Assess the morphology of the red blood cells.
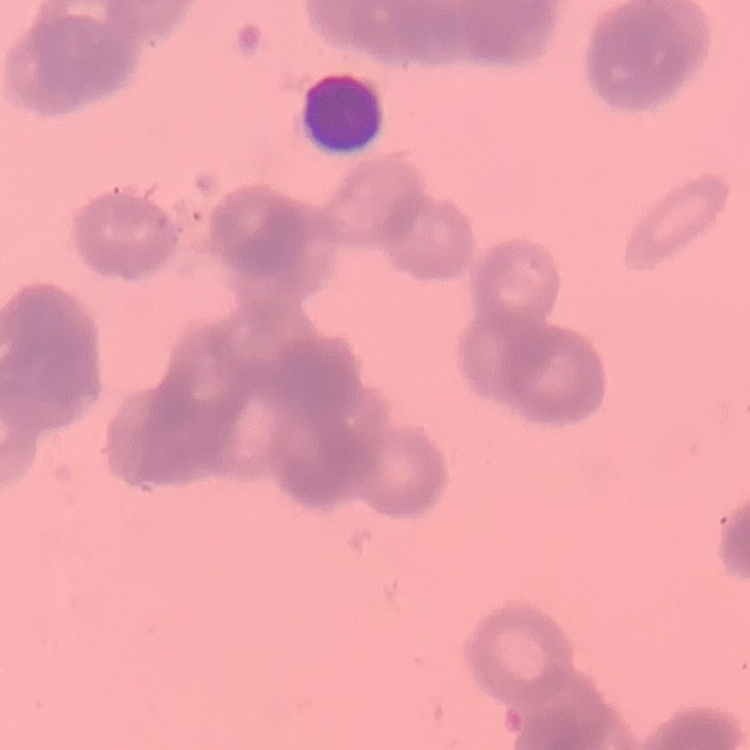
Rouleaux formation.

{
  "stain": "Field's or Giemsa",
  "preparation": "thin peripheral smear",
  "image_type": "square crop of a larger photomicrograph"
}